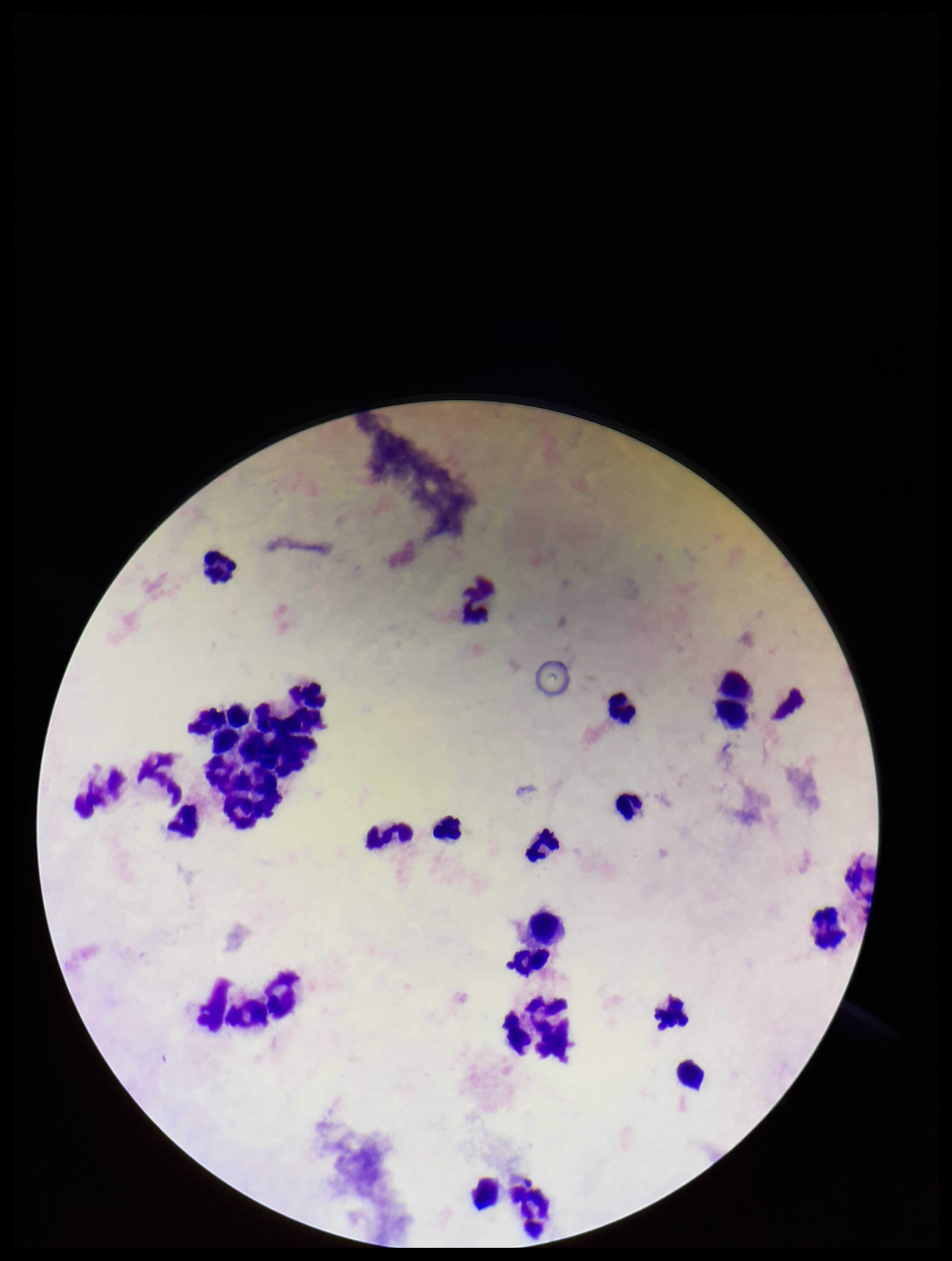

parasite count = 0
Plasmodium parasites = none detected
field of view = one from this slide
image size = 952×1261 pixels
preparation = thick smear
leukocyte count = 27
capture = smartphone photograph through the microscope eyepiece
stain = Giemsa
patient malaria status = negative